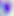
Summary:
  - Modality: photomicrograph
  - Magnification: 400x
  - Identification: Toxoplasma gondii